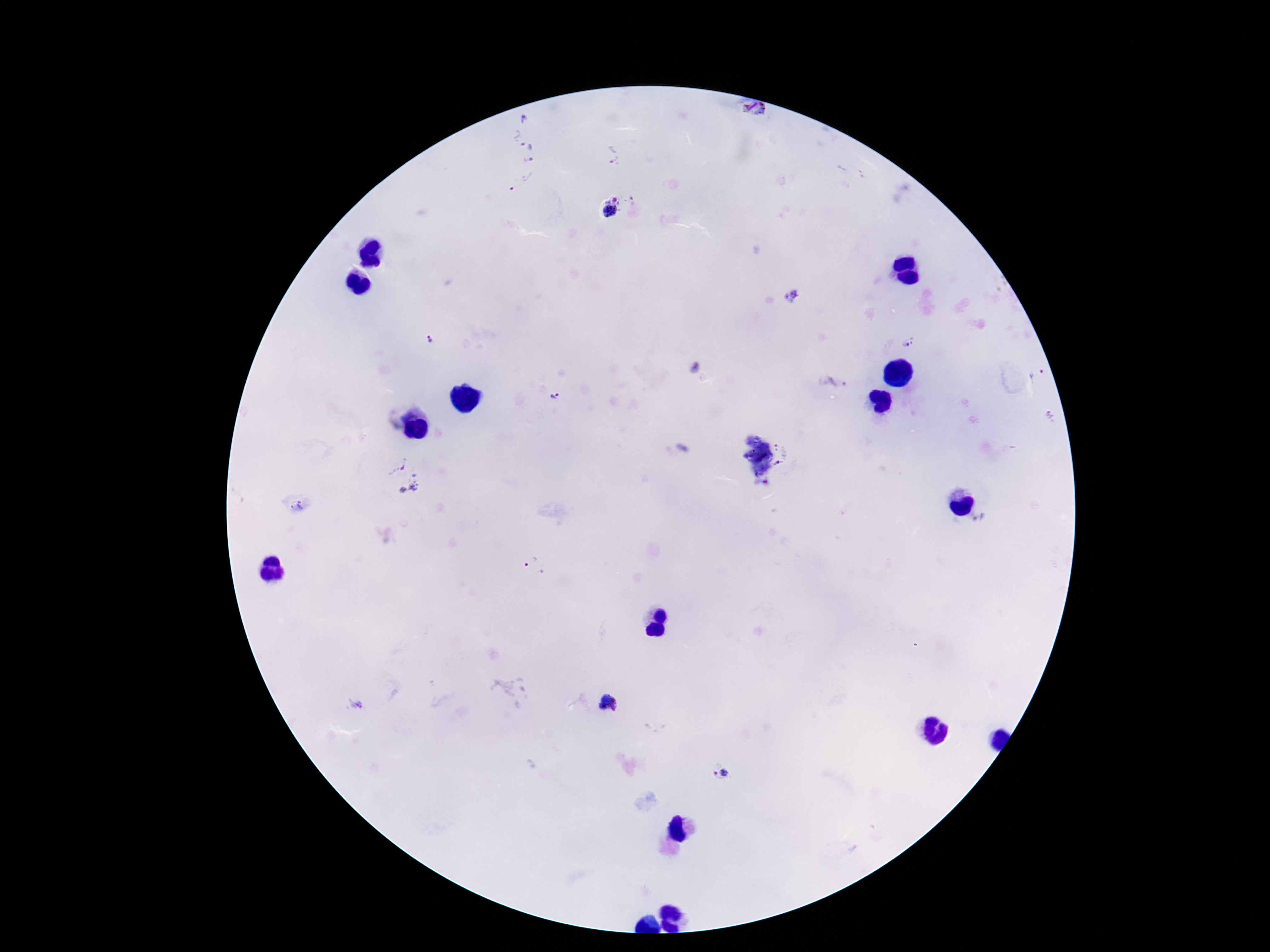
magnification: 100x
patient_malaria_status: positive
field_of_view: one from this slide
preparation: thick blood film
image_size: 1270×952 pixels
capture: smartphone camera through the microscope eyepiece
stain: Giemsa
plasmodium_parasite_locations: 'approximate centers as {x, y} in pixels: {756, 113}, {524, 119}, {525, 146}, {612, 156}, {523, 183}, {611, 208}, {791, 295}, {428, 341}, {909, 344}, {695, 368}, {1036, 375}, {833, 382}, {552, 396}, {1052, 418}, {783, 448}, {682, 449}, {778, 465}, {401, 477}, {300, 507}, {534, 566}, {721, 774}'